Assess this cell for malaria.
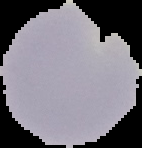

Uninfected.

preparation: thin blood smear
image_size: 142×148 pixels
image_type: segmented cell region on a black background